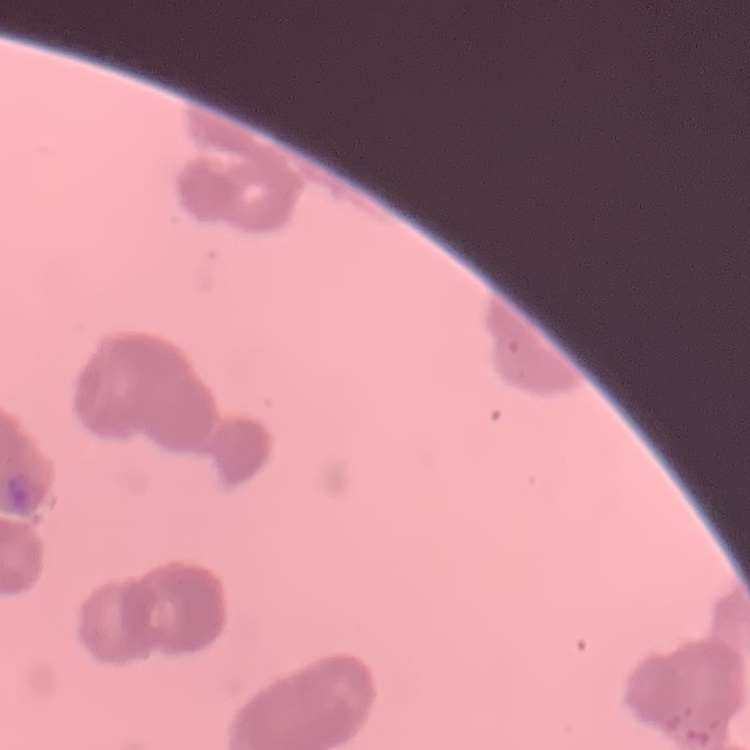
Summary:
  - Erythrocyte morphology: rouleaux formation
  - Preparation: thin peripheral smear
  - Image type: square crop of a larger photomicrograph
  - Stain: Field's or Giemsa